Point out every Plasmodium parasite.
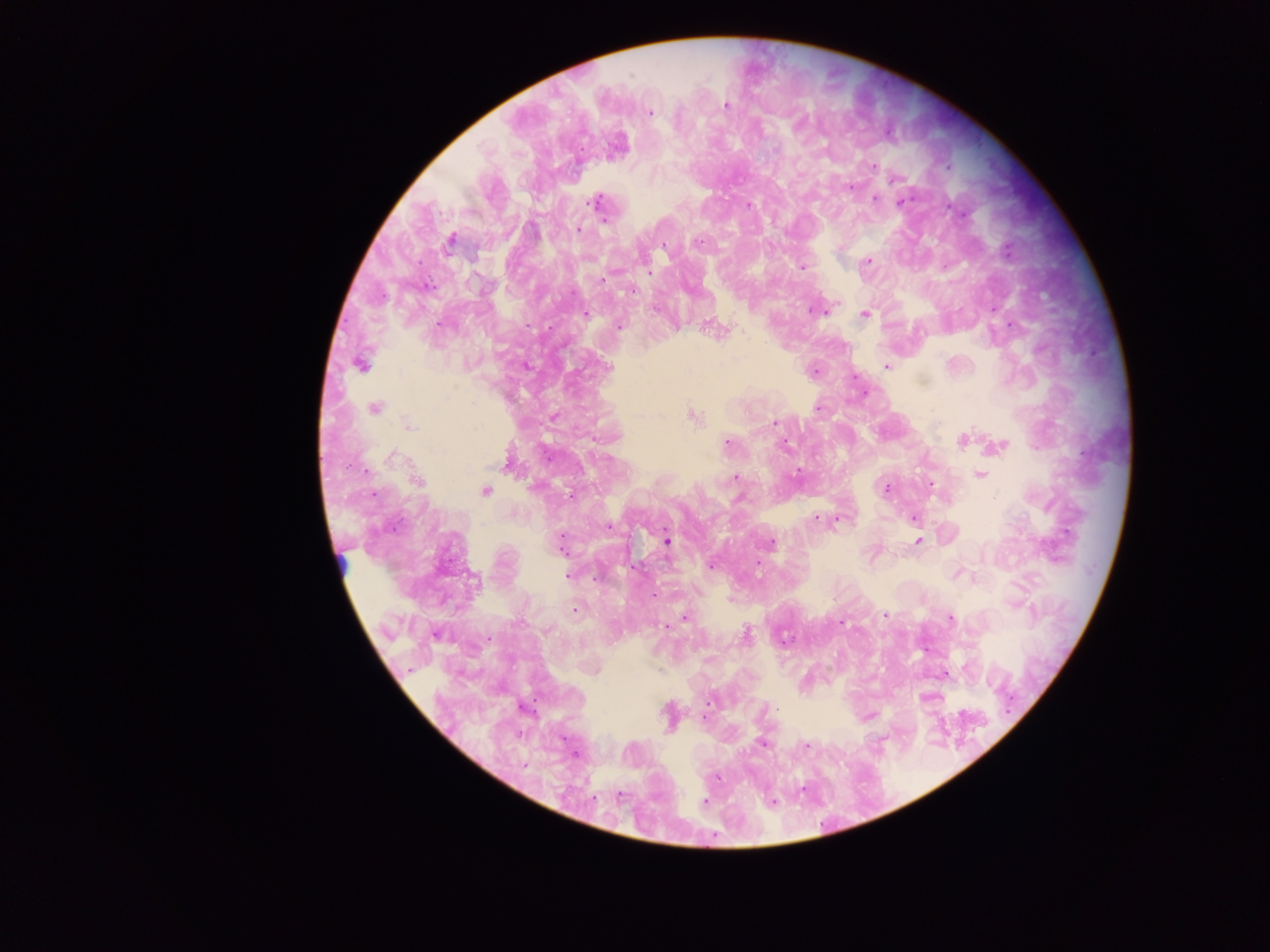
Approximate centers as [x, y] in pixels.
Plasmodium parasites: [725, 105], [649, 112], [889, 131], [873, 167], [850, 186], [874, 198], [901, 200], [596, 202], [578, 229], [450, 239], [697, 242], [664, 244], [867, 261], [801, 266], [601, 280], [632, 290], [816, 308], [865, 314], [1011, 324], [619, 326], [712, 328], [360, 364], [525, 366], [886, 366], [609, 368], [814, 369], [375, 408], [817, 408], [691, 415], [774, 422], [407, 424], [961, 439], [727, 442], [783, 445], [998, 446], [390, 456], [509, 462], [980, 474], [735, 477], [415, 480], [931, 485], [885, 488], [484, 491], [815, 518], [839, 518], [914, 518], [666, 541], [917, 541], [770, 543], [561, 545], [757, 563], [711, 565], [567, 575], [655, 596], [574, 609], [884, 614], [685, 617], [949, 617], [841, 622], [666, 626], [745, 635], [943, 674], [710, 699], [868, 716], [668, 718], [704, 718], [763, 743], [575, 754], [704, 802].

Mobile-phone photograph taken through the microscope. Image is 1270×952 pixels. Sample from Ghana. One field of view. Thick blood smear.